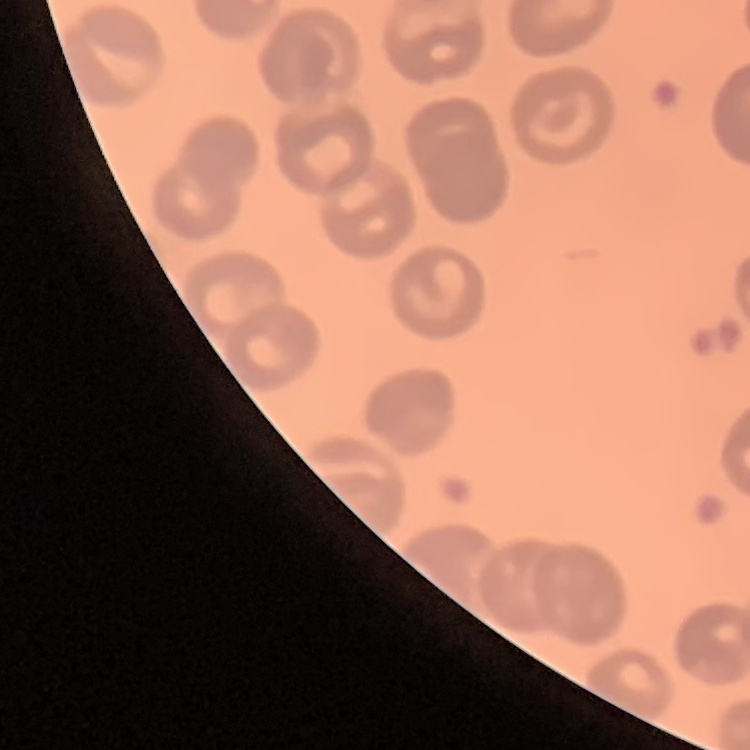
{
  "red_blood_cell_morphology": "no rouleaux formation",
  "image_type": "one tile cut from a larger photomicrograph",
  "preparation": "thin blood smear",
  "stain": "Field's or Giemsa"
}